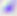

Toxoplasma gondii is seen. 400x magnification. Micrograph.